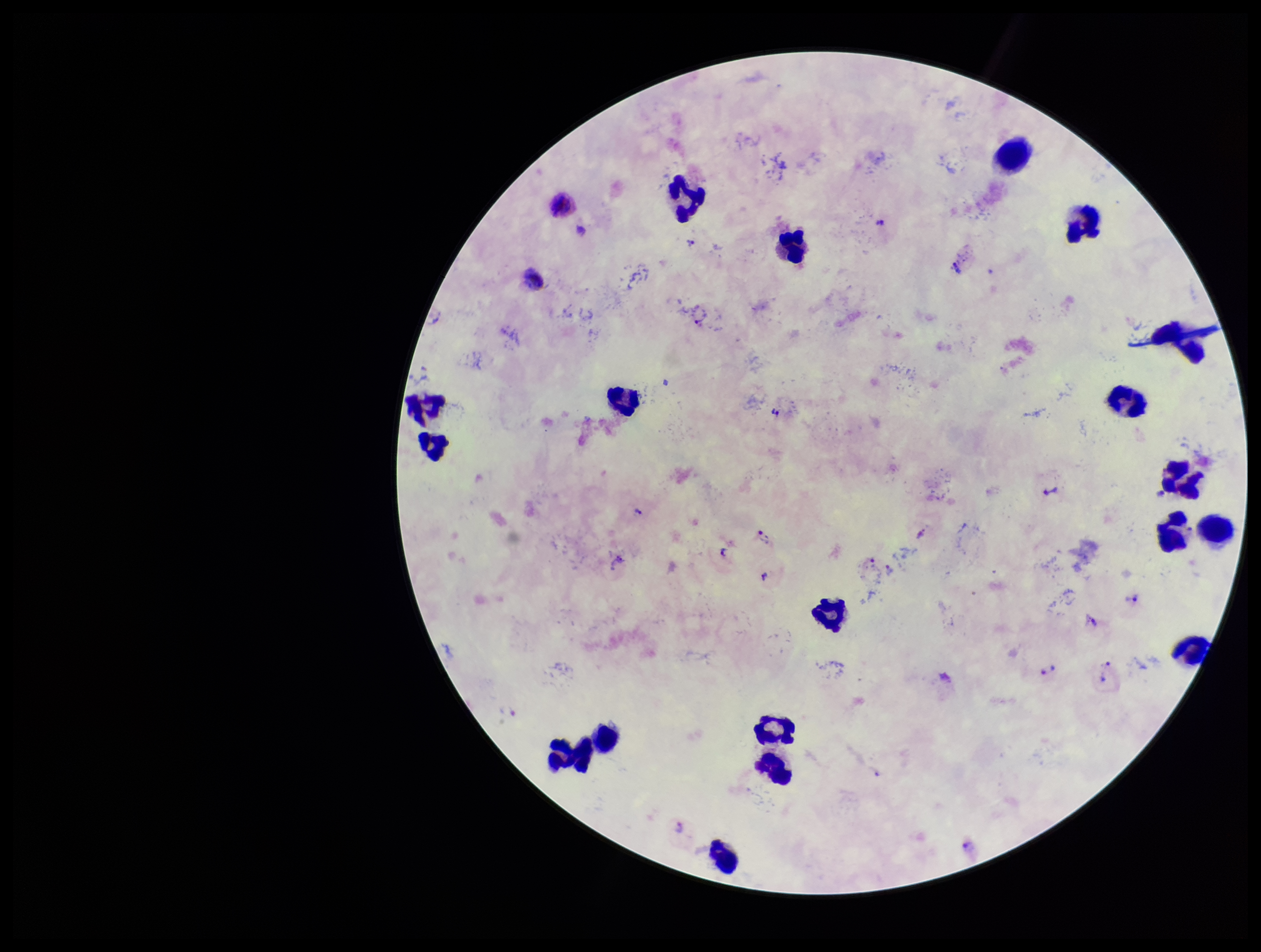

parasite count = 10
stain = Giemsa
Plasmodium parasites = seen
capture = smartphone photograph through the microscope eyepiece
preparation = thick blood smear
species reported for this patient = Plasmodium vivax
leukocyte count = 19
patient malaria status = positive
image size = 1261×952 pixels
field of view = single